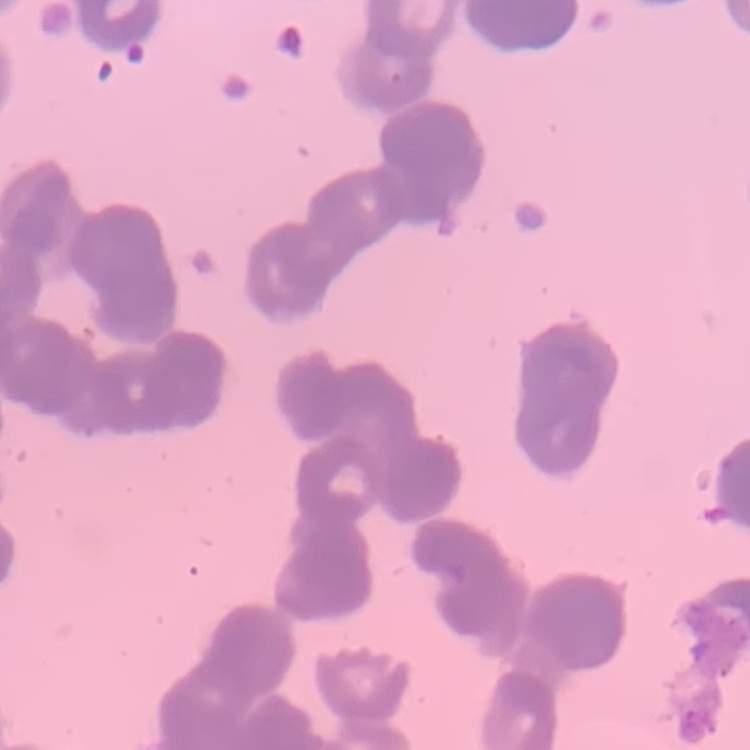
Summary:
  - Erythrocyte morphology: rouleaux formation
  - Stain: Field's or Giemsa
  - Image type: one tile cut from a larger photomicrograph
  - Preparation: thin peripheral smear